State which parasite is depicted.
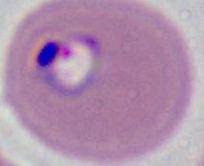

Plasmodium.

{
  "magnification": "400x or 1000x",
  "modality": "photomicrograph"
}